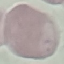

Summary:
  - Result: negative for malaria parasites
  - Capture: smartphone through the microscope eyepiece
  - Image type: automatically extracted cell patch, resized to 64 × 64 pixels
  - Preparation: thin blood film
  - Stain: Giemsa